Locate every Plasmodium parasite.
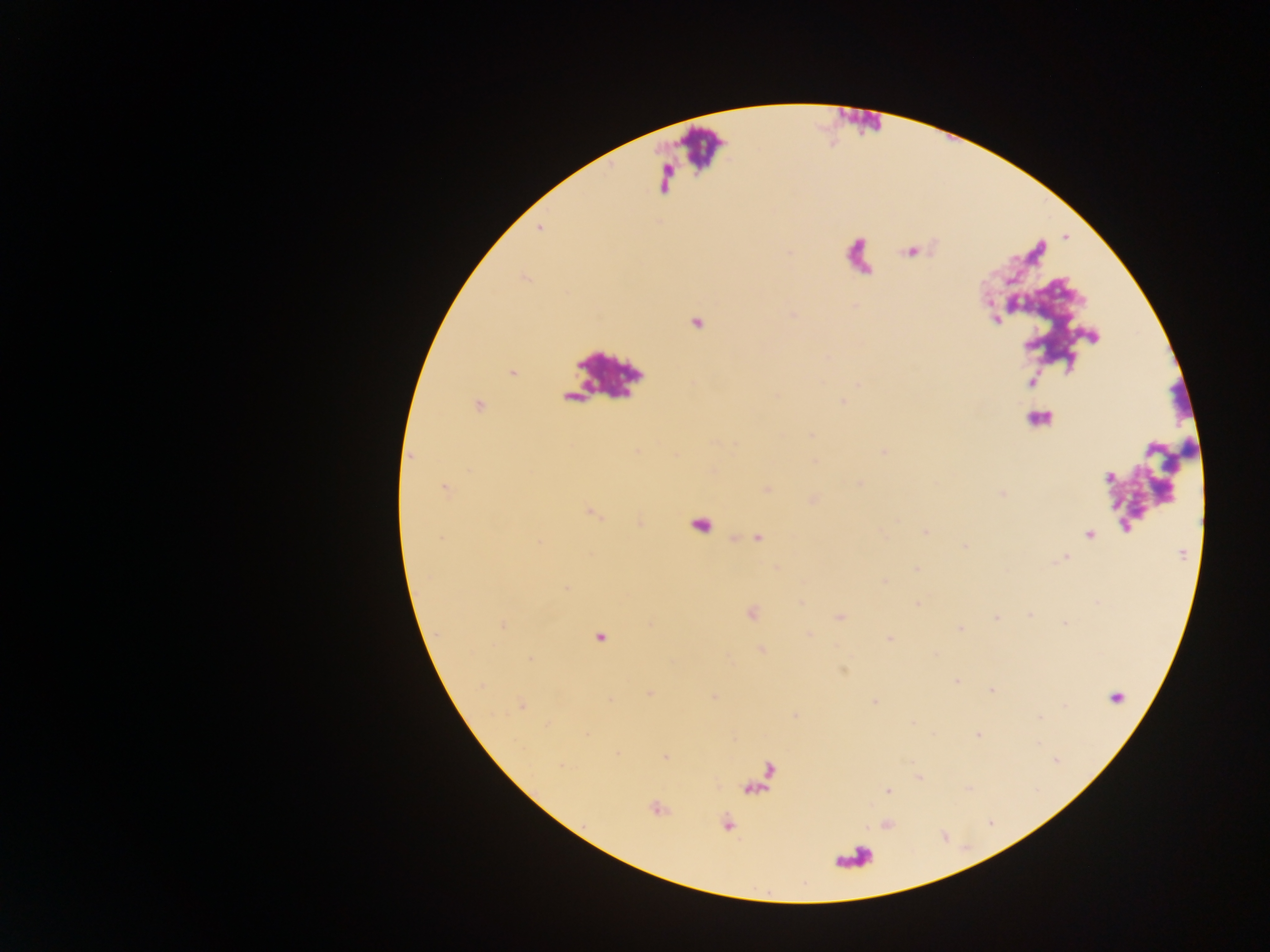

Approximate centers as [x, y] in pixels.
Plasmodium parasites: [541, 227], [790, 250], [910, 250], [995, 320], [1096, 339], [513, 372], [842, 402], [413, 458], [443, 488], [593, 515], [926, 532], [1088, 534], [757, 537], [1182, 554], [1065, 558], [914, 568], [882, 582], [565, 588], [916, 603], [838, 615], [1029, 615], [994, 616], [1065, 624], [503, 626], [959, 629], [889, 639], [760, 650], [531, 659], [843, 671], [956, 679], [991, 691], [649, 693], [715, 695], [874, 703], [521, 706], [1039, 718], [914, 723], [977, 736], [1037, 742], [617, 754], [664, 756], [561, 765], [887, 789], [656, 807], [728, 822].

Leukocyte locations: [699, 144]. One field of view. Thick blood smear. Image is 1270×952 pixels. Mobile-phone photograph taken through the microscope. Collected in Ghana.